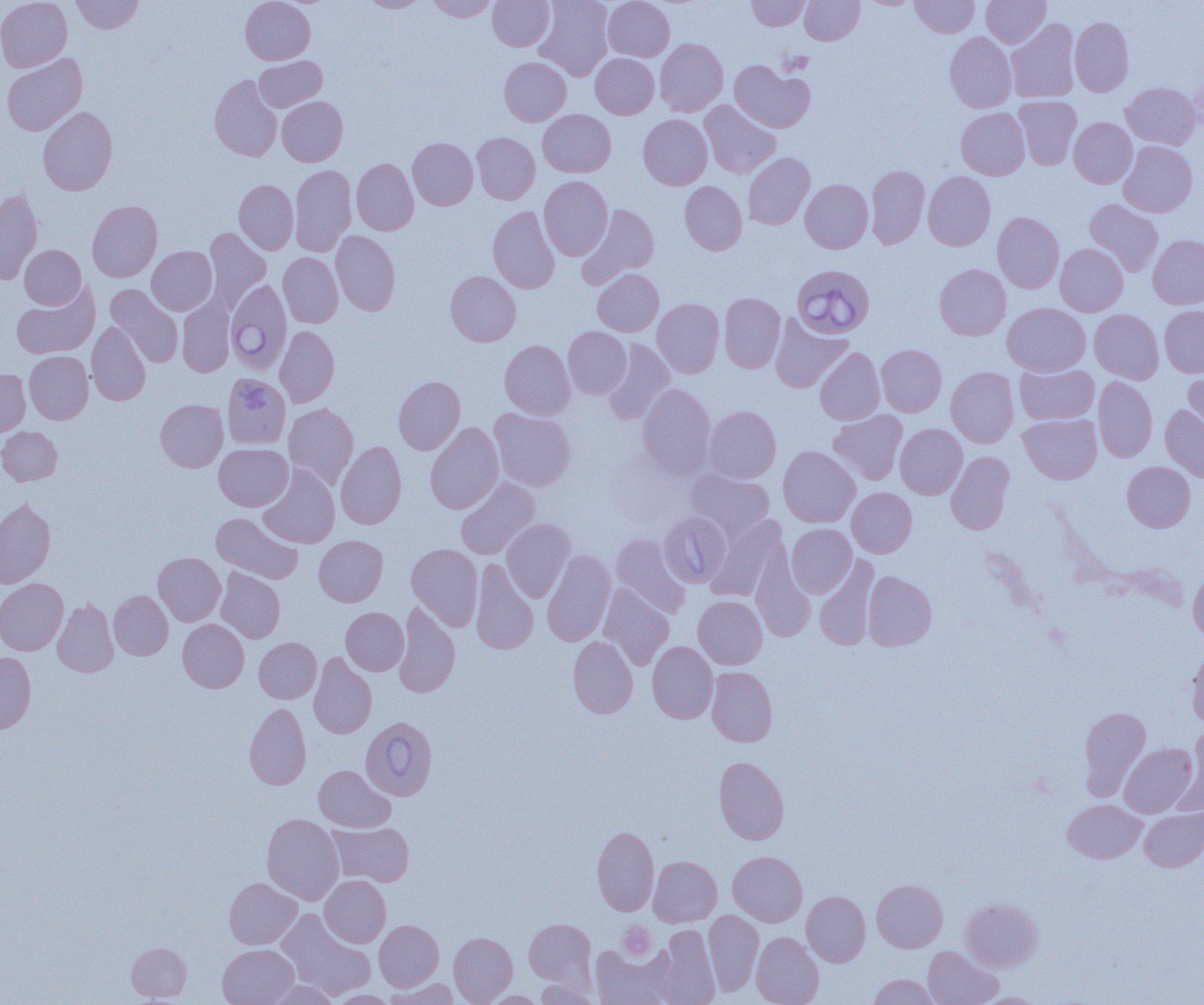

slide_level_diagnosis: Babesia divergens
preparation: thin blood smear
uninfected_red_blood_cell_locations: 'approximate bounding boxes as [x1, y1, x2, y2] in pixels: [0, 0, 72, 72], [71, 0, 143, 34], [240, 0, 315, 64], [359, 0, 427, 12], [426, 0, 498, 21], [488, 0, 554, 50], [535, 0, 614, 81], [603, 0, 675, 61], [747, 0, 811, 31], [800, 0, 864, 45], [910, 0, 979, 37], [981, 0, 1050, 48], [1070, 17, 1134, 96], [1006, 19, 1079, 103], [945, 32, 1016, 112], [655, 38, 728, 116], [2, 53, 88, 136], [590, 54, 659, 118], [254, 56, 327, 111], [499, 57, 571, 126], [730, 60, 815, 132], [209, 74, 282, 161], [1121, 83, 1201, 149], [277, 96, 348, 166], [1014, 96, 1081, 169], [699, 100, 780, 178], [38, 106, 118, 195], [956, 107, 1030, 180], [538, 109, 616, 177], [638, 114, 712, 189], [1069, 118, 1137, 188], [472, 132, 539, 204], [408, 137, 478, 210], [1118, 140, 1198, 217], [743, 152, 815, 229], [352, 159, 418, 235], [290, 165, 356, 256], [866, 165, 929, 249], [923, 171, 995, 250], [539, 176, 613, 260], [800, 179, 873, 253], [234, 180, 298, 254], [680, 181, 747, 255], [0, 188, 43, 284], [1084, 199, 1163, 277], [87, 200, 162, 282], [578, 204, 659, 287], [487, 206, 560, 293], [992, 212, 1064, 293], [203, 227, 271, 313], [331, 231, 400, 315], [1148, 234, 1204, 309], [1055, 244, 1128, 316], [20, 245, 85, 309], [147, 246, 217, 315], [278, 252, 343, 327], [934, 264, 1010, 340], [593, 269, 663, 336], [445, 271, 521, 346], [12, 283, 100, 359], [106, 284, 183, 367], [719, 293, 785, 373], [177, 296, 235, 377], [652, 298, 724, 378], [1003, 303, 1091, 375], [1159, 305, 1204, 377], [1090, 309, 1164, 383], [770, 316, 852, 392], [86, 322, 151, 405], [274, 326, 340, 407], [563, 326, 632, 399], [602, 339, 675, 424], [500, 340, 575, 419], [876, 345, 946, 416], [815, 347, 884, 425], [24, 351, 93, 423], [1015, 363, 1099, 424], [946, 366, 1019, 448], [1184, 368, 1204, 442], [0, 369, 30, 436], [224, 375, 295, 454], [394, 376, 465, 454], [1093, 376, 1157, 462], [636, 383, 716, 479], [155, 399, 228, 472], [283, 403, 358, 489], [1160, 405, 1204, 482], [703, 406, 781, 482], [489, 408, 576, 491], [828, 410, 907, 484], [1018, 414, 1102, 484], [425, 422, 504, 514], [895, 423, 968, 499], [0, 427, 62, 485], [336, 441, 406, 528], [214, 443, 292, 511], [778, 446, 860, 527], [946, 451, 1014, 535], [1122, 461, 1195, 532], [258, 464, 340, 548], [687, 469, 774, 538], [456, 476, 539, 559], [847, 487, 917, 557], [0, 497, 56, 588], [211, 512, 303, 584], [705, 516, 788, 601], [501, 518, 576, 602], [786, 524, 857, 597], [611, 534, 690, 618], [314, 535, 388, 606], [407, 543, 483, 630], [542, 550, 616, 646], [153, 552, 225, 625], [751, 553, 815, 642], [814, 555, 878, 651], [470, 559, 538, 655], [216, 568, 285, 643], [1187, 570, 1204, 643], [862, 571, 937, 650], [0, 578, 68, 655], [598, 584, 674, 670], [109, 590, 173, 660], [693, 596, 767, 669], [52, 598, 119, 677], [394, 602, 460, 698], [341, 607, 408, 675], [177, 619, 249, 692], [568, 636, 637, 718], [254, 637, 321, 703], [647, 641, 718, 723], [1186, 648, 1204, 729], [0, 652, 36, 734], [309, 653, 377, 738], [707, 667, 777, 746], [245, 702, 311, 790], [1078, 706, 1151, 800], [1182, 725, 1204, 811], [1119, 743, 1198, 817], [714, 756, 789, 844], [314, 765, 395, 832], [1063, 799, 1146, 863], [1140, 807, 1204, 872], [261, 813, 344, 904], [327, 822, 413, 887], [592, 826, 659, 916], [728, 851, 807, 926], [649, 856, 721, 926], [320, 875, 390, 947], [224, 877, 302, 949], [872, 879, 947, 952], [802, 891, 870, 967], [961, 897, 1042, 972], [276, 909, 375, 1000], [703, 909, 763, 996], [524, 918, 596, 988], [375, 920, 443, 991], [653, 925, 721, 1005], [374, 928, 518, 994], [751, 931, 823, 1005], [449, 932, 517, 1004], [126, 942, 191, 1002], [589, 943, 677, 1005], [218, 944, 299, 1005], [923, 946, 1002, 1005], [869, 974, 938, 1004], [535, 976, 600, 1005], [385, 978, 459, 1004], [262, 979, 339, 1005], [325, 990, 398, 1004], [483, 991, 548, 1004]'
platelet_locations: 'approximate bounding boxes as [x1, y1, x2, y2] in pixels: [777, 49, 813, 76], [618, 922, 655, 960]'
babesia_divergens_infected_red_blood_cell_locations: 'approximate bounding boxes as [x1, y1, x2, y2] in pixels: [794, 267, 875, 341], [226, 278, 292, 375], [659, 512, 732, 588], [361, 717, 437, 800]'
modality: light microscopy
image_size: 1204×1005 pixels
field_of_view: single
magnification: 1000x